Assess this cell for malaria.
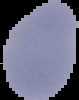

Uninfected.

Summary:
  - Image type: segmented cell region on a black background
  - Preparation: thin blood smear
  - Image size: 79×100 pixels